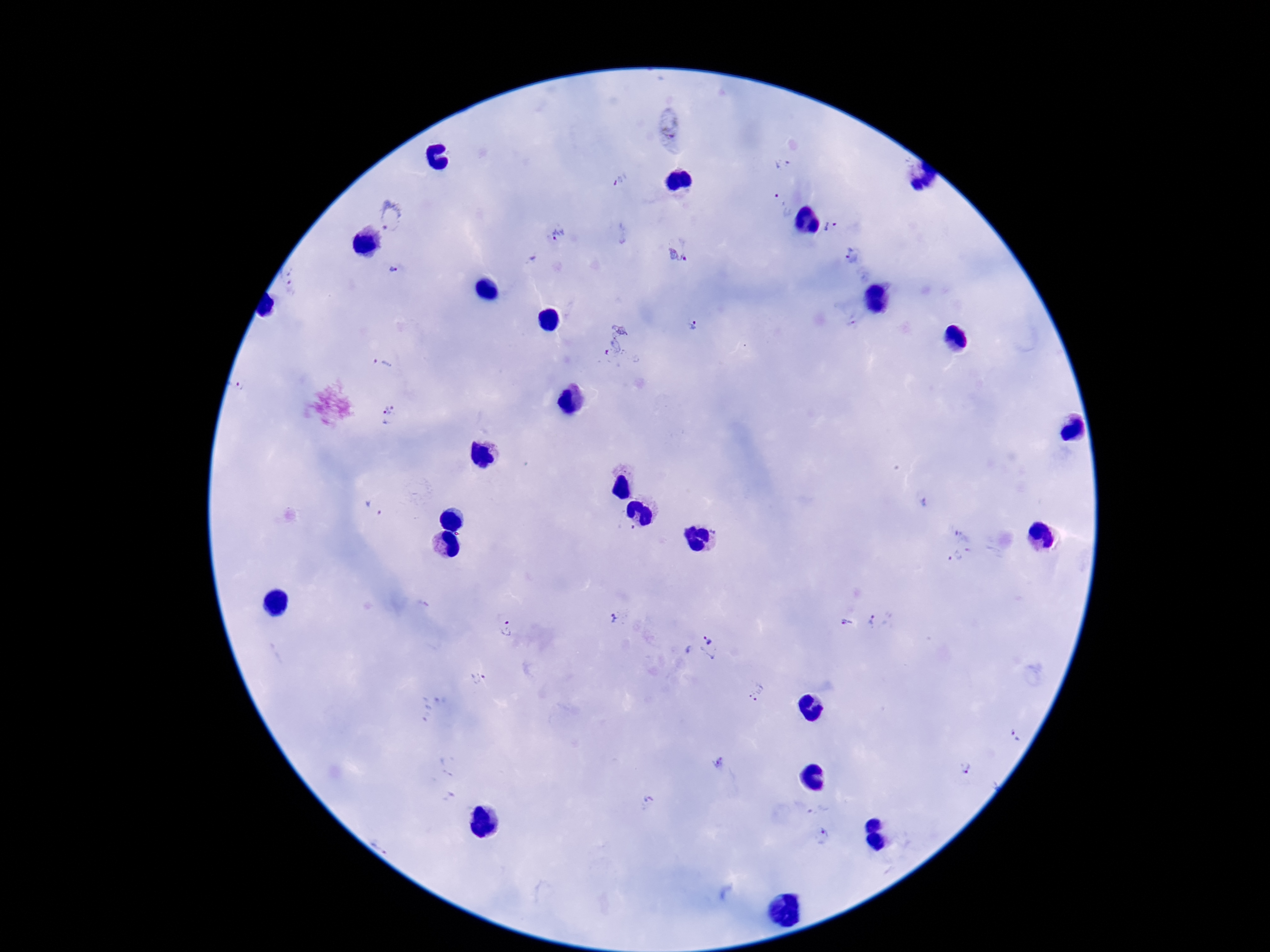

Approximate centers as (x, y) in pixels. Plasmodium parasite locations: (669, 131), (784, 165), (621, 180), (782, 205), (392, 218), (831, 226), (558, 234), (679, 251), (852, 256), (533, 259), (394, 270), (290, 288), (692, 325), (615, 340), (383, 363), (240, 386), (390, 416), (373, 508), (626, 528), (964, 536), (959, 558), (612, 618), (880, 620), (845, 623), (505, 629), (701, 648), (478, 677), (757, 691), (1015, 735), (719, 764), (966, 768), (648, 802), (818, 809), (821, 837). Image is 1270×952 pixels. Thick blood smear. Photographed through the microscope eyepiece with a smartphone camera. One field from this slide. Giemsa stain. Patient malaria status: infected. 100x magnification.